Describe the morphology of the erythrocytes.
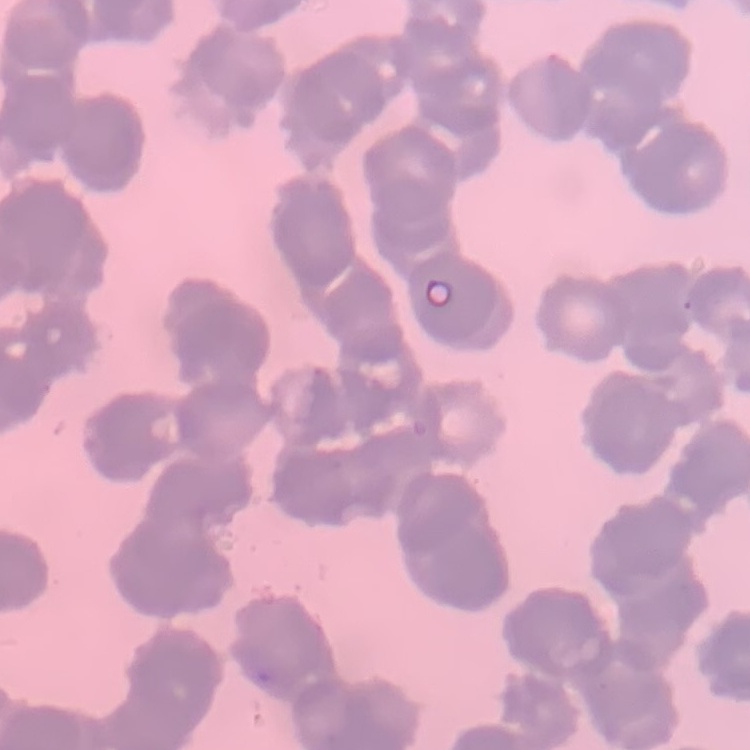

Rouleaux formation.

{
  "stain": "Field's or Giemsa",
  "image_type": "square crop of a larger photomicrograph",
  "preparation": "thin blood smear"
}